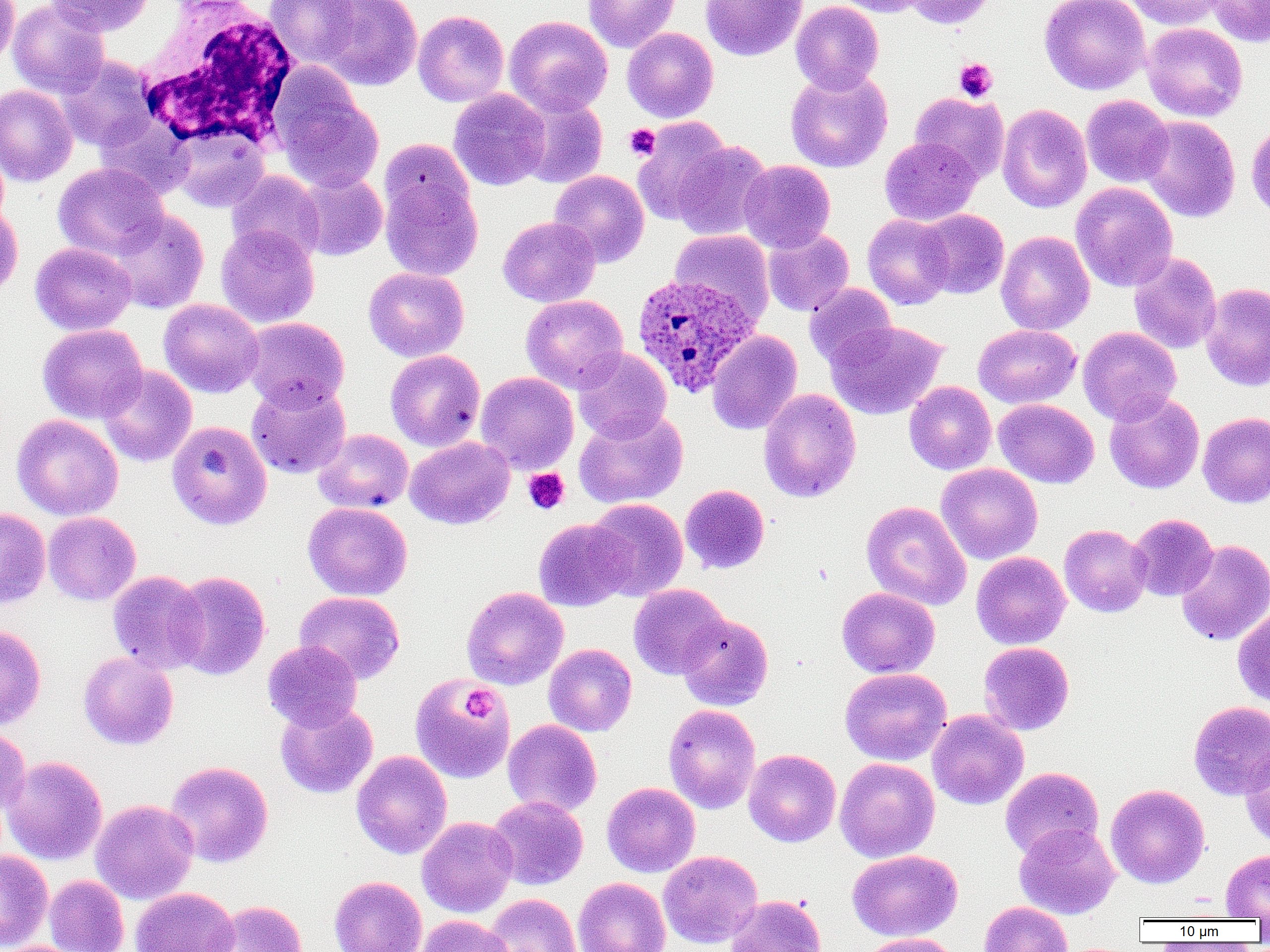
Summary:
  - Coordinate format: approximate bounding boxes as [x1, y1, x2, y2] in pixels
  - Plasmodium ovale-infected red blood cell locations: [631, 274, 759, 398]
  - White blood cell locations: [135, 2, 300, 150]
  - Platelet locations: [954, 58, 998, 101], [624, 124, 660, 160], [523, 468, 570, 515], [462, 687, 496, 722]
  - Uninfected red blood cell locations: [0, 0, 19, 69], [8, 0, 109, 99], [44, 0, 154, 36], [264, 0, 364, 68], [314, 0, 422, 91], [583, 0, 680, 52], [700, 0, 807, 61], [832, 0, 926, 17], [902, 0, 996, 28], [1039, 0, 1151, 95], [1126, 0, 1225, 30], [1208, 0, 1270, 46], [791, 1, 884, 94], [413, 10, 509, 107], [504, 16, 613, 116], [1142, 22, 1248, 122], [622, 27, 719, 123], [58, 55, 157, 151], [785, 69, 892, 172], [272, 76, 384, 193], [0, 84, 77, 186], [448, 89, 550, 190], [910, 92, 1009, 182], [1081, 94, 1173, 187], [516, 95, 608, 189], [997, 104, 1092, 213], [95, 115, 196, 200], [1139, 115, 1240, 222], [633, 117, 733, 225], [1245, 120, 1270, 221], [170, 126, 270, 213], [879, 136, 981, 225], [671, 140, 773, 240], [739, 160, 835, 252], [53, 162, 169, 260], [379, 162, 484, 282], [226, 170, 324, 263], [549, 170, 650, 267], [295, 171, 387, 261], [1071, 182, 1178, 293], [0, 202, 23, 303], [106, 209, 210, 313], [916, 209, 1009, 299], [862, 214, 953, 309], [498, 216, 600, 307], [216, 225, 319, 328], [763, 228, 854, 316], [670, 230, 774, 325], [996, 230, 1095, 335], [30, 242, 137, 335], [1128, 252, 1221, 354], [363, 267, 469, 362], [1200, 282, 1270, 392], [804, 283, 898, 370], [521, 294, 628, 393], [158, 299, 264, 397], [242, 317, 349, 411], [827, 320, 947, 419], [37, 324, 147, 423], [973, 324, 1081, 408], [1078, 326, 1182, 424], [707, 330, 803, 435], [572, 348, 672, 443], [385, 350, 485, 451], [97, 364, 196, 467], [476, 372, 579, 474], [246, 380, 351, 479], [904, 381, 996, 475], [759, 388, 861, 502], [902, 388, 1099, 478], [1104, 392, 1204, 494], [994, 399, 1098, 488], [574, 410, 688, 508], [1197, 412, 1270, 508], [11, 414, 123, 520], [167, 420, 272, 530], [313, 428, 413, 514], [405, 436, 515, 529], [936, 463, 1043, 564], [680, 484, 770, 574], [587, 498, 688, 600], [861, 501, 971, 611], [303, 502, 412, 601], [0, 507, 50, 609], [43, 512, 141, 605], [1129, 513, 1218, 601], [533, 518, 632, 611], [1059, 524, 1152, 617], [1176, 539, 1270, 646], [971, 551, 1070, 649], [107, 570, 209, 674], [169, 570, 270, 680], [629, 584, 730, 679], [461, 586, 568, 690], [837, 587, 940, 678], [294, 591, 405, 683], [1233, 606, 1270, 708], [677, 613, 773, 711], [0, 624, 46, 729], [262, 640, 362, 731], [978, 642, 1074, 735], [544, 644, 637, 736], [78, 652, 179, 750], [839, 667, 951, 765], [410, 674, 515, 784], [275, 701, 378, 799], [1189, 701, 1270, 798], [663, 703, 761, 814], [927, 710, 1029, 809], [503, 719, 602, 817], [0, 725, 31, 817], [1240, 745, 1270, 847], [743, 749, 841, 847], [352, 750, 452, 859], [2, 755, 107, 865], [835, 757, 940, 862], [165, 760, 273, 867], [1000, 767, 1104, 860], [601, 782, 700, 877], [1106, 784, 1209, 888], [487, 796, 588, 890], [90, 799, 199, 904], [417, 816, 518, 917], [1014, 823, 1120, 919], [0, 849, 53, 951], [847, 849, 962, 941], [1221, 849, 1270, 920], [658, 850, 763, 948], [44, 875, 129, 952], [329, 876, 426, 952], [573, 877, 671, 952], [131, 887, 239, 952], [485, 893, 581, 952], [726, 894, 826, 952], [205, 900, 308, 951], [979, 900, 1072, 952], [415, 914, 515, 952], [861, 933, 959, 952]
  - Slide-level diagnosis: Plasmodium ovale
  - Preparation: thin blood smear
  - Modality: light microscopy
  - Field of view: one of a larger specimen
  - Magnification: 1000x
  - Image size: 1270×952 pixels